Classify this cell by malaria status.
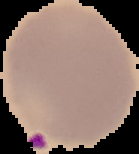

It is parasitized.

Cell region segmented out of the field of view; the surrounding area is masked to black. From a thin blood smear. Image is 139×154 pixels.